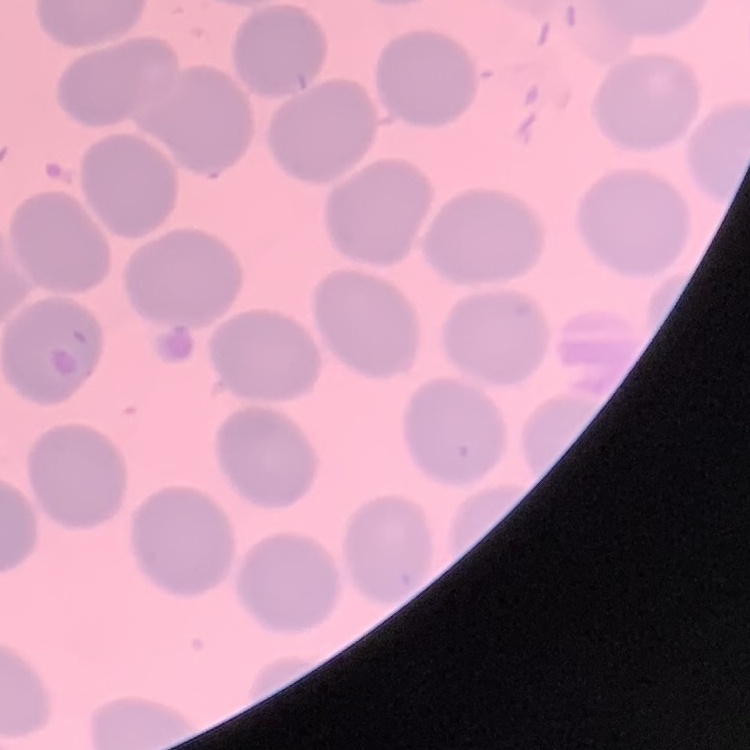 The erythrocytes exhibit no rouleaux formation. Stained with either Field's or Giemsa. One tile cut from a larger photomicrograph. Thin blood film.